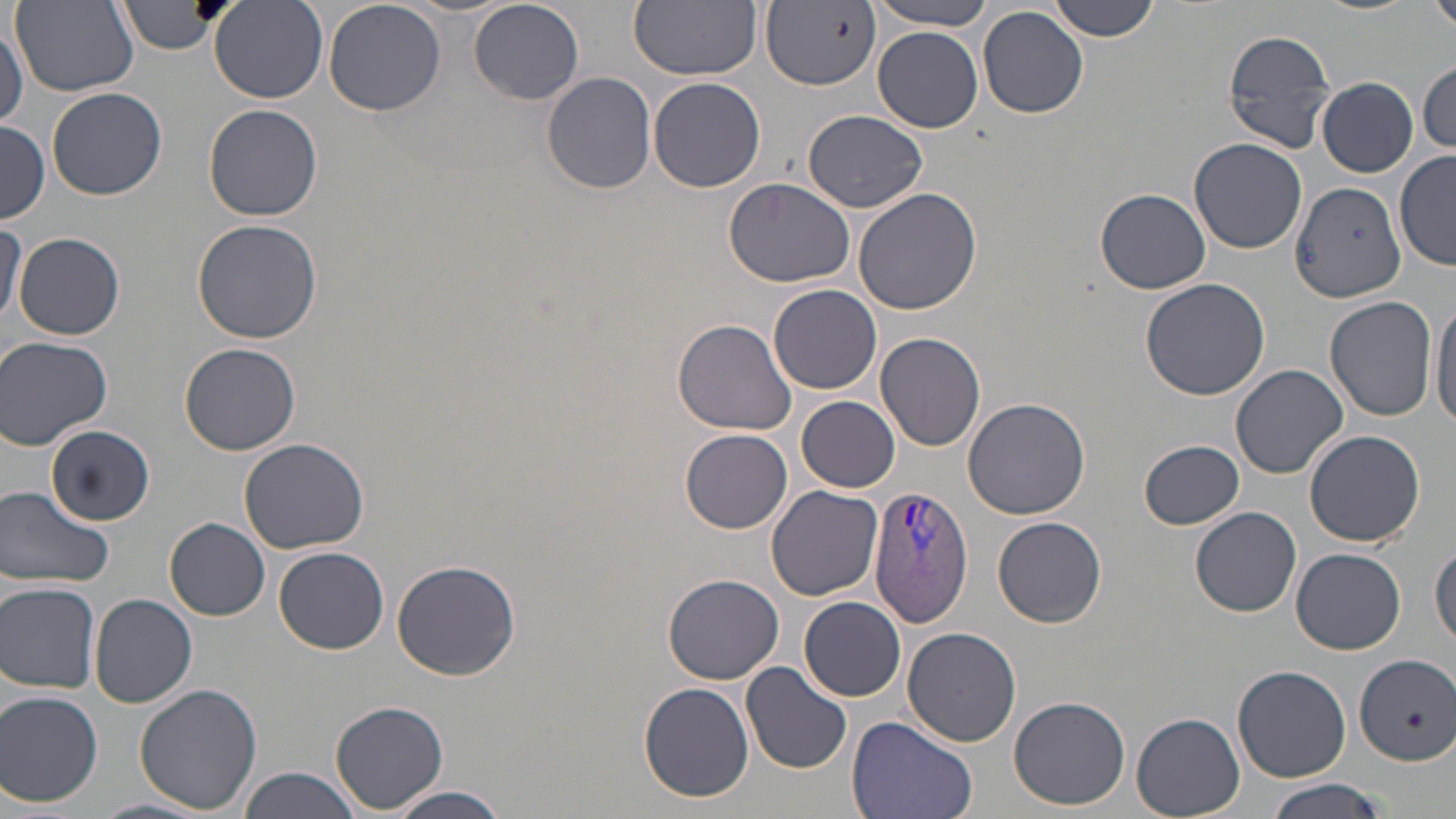
Summary:
  - Coordinate format: approximate bounding boxes as [x1, y1, x2, y2] in pixels
  - Uninfected red blood cell locations: [119, 0, 225, 55], [323, 0, 447, 115], [469, 0, 584, 105], [631, 0, 762, 80], [869, 0, 993, 30], [1046, 0, 1162, 41], [1426, 0, 1456, 37], [209, 1, 328, 103], [13, 3, 142, 96], [762, 3, 880, 91], [977, 7, 1089, 119], [1, 20, 26, 129], [873, 27, 985, 131], [1222, 27, 1338, 152], [1416, 59, 1454, 154], [542, 72, 657, 193], [647, 76, 766, 193], [1318, 77, 1417, 176], [46, 86, 166, 201], [203, 105, 323, 221], [804, 110, 927, 213], [0, 122, 49, 222], [1189, 138, 1307, 254], [1394, 150, 1455, 270], [725, 177, 855, 288], [1291, 179, 1407, 302], [853, 187, 984, 317], [1097, 188, 1209, 293], [192, 217, 324, 344], [0, 223, 26, 329], [15, 233, 125, 341], [1140, 277, 1272, 401], [770, 283, 882, 394], [1430, 295, 1456, 435], [1325, 296, 1439, 421], [672, 317, 800, 437], [875, 332, 986, 451], [0, 337, 113, 451], [180, 343, 302, 456], [1231, 364, 1349, 477], [795, 396, 901, 492], [963, 397, 1091, 519], [47, 425, 154, 525], [682, 428, 793, 531], [1304, 429, 1427, 546], [237, 437, 369, 553], [1139, 440, 1245, 529], [0, 485, 113, 590], [767, 485, 883, 601], [1190, 507, 1302, 617], [994, 516, 1106, 627], [165, 517, 272, 619], [1431, 543, 1455, 650], [274, 546, 390, 655], [1291, 548, 1405, 654], [391, 560, 523, 681], [662, 573, 784, 683], [0, 581, 102, 694], [89, 593, 197, 708], [799, 597, 906, 701], [903, 626, 1021, 748], [1355, 654, 1456, 765], [742, 661, 852, 773], [1232, 664, 1352, 783], [638, 680, 755, 804], [133, 682, 260, 814], [0, 690, 104, 806], [1008, 694, 1130, 810], [331, 700, 448, 812], [1132, 712, 1245, 816], [846, 715, 980, 819], [238, 766, 365, 819], [1264, 778, 1389, 819], [382, 785, 512, 819], [94, 796, 210, 819]
  - Plasmodium vivax-infected red blood cell locations: [869, 486, 974, 625]
  - Slide-level diagnosis: Plasmodium vivax
  - Field of view: one of a larger specimen
  - Image size: 1456×819 pixels
  - Magnification: 1000x
  - Modality: light microscopy
  - Stain: May-Grünwald-Giemsa
  - Preparation: thin blood film